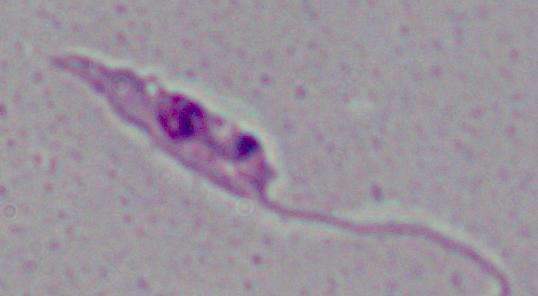 1000x magnification. A Leishmania parasite is shown. Micrograph.